Comment on the morphology of the erythrocytes.
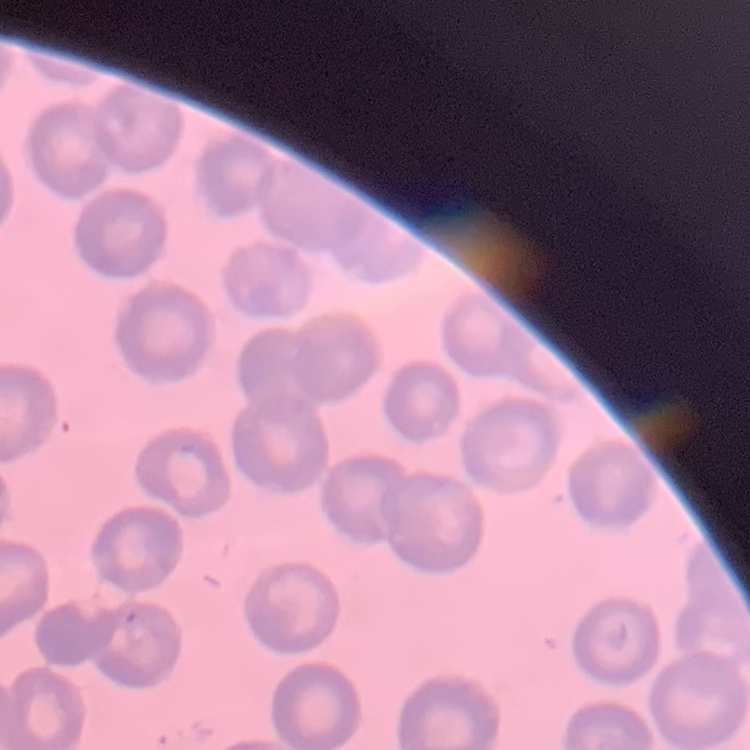
They show no rouleaux formation.

Thin peripheral smear. Stained with either Field's or Giemsa. One tile cut from a larger photomicrograph.